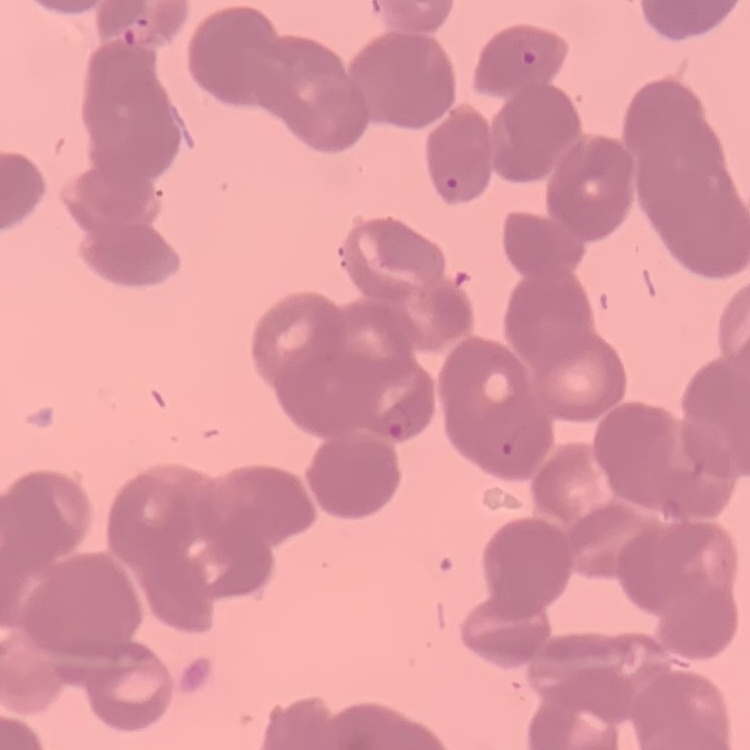

Summary:
  - Erythrocyte morphology: rouleaux formation
  - Stain: Field's or Giemsa
  - Image type: square crop of a larger photomicrograph
  - Preparation: thin peripheral smear